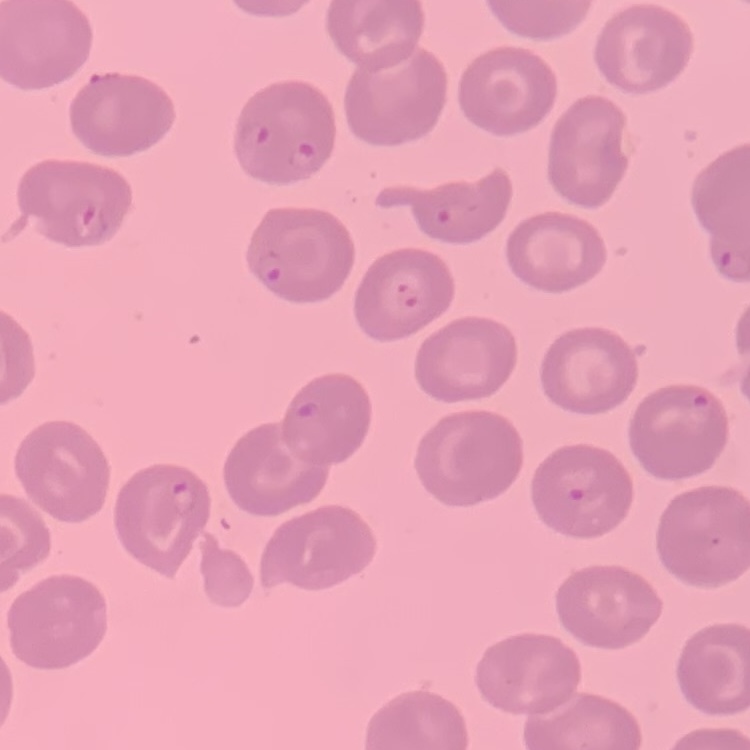

red blood cell morphology = no rouleaux formation
preparation = thin blood smear
stain = Field's or Giemsa
image type = square crop of a larger photomicrograph